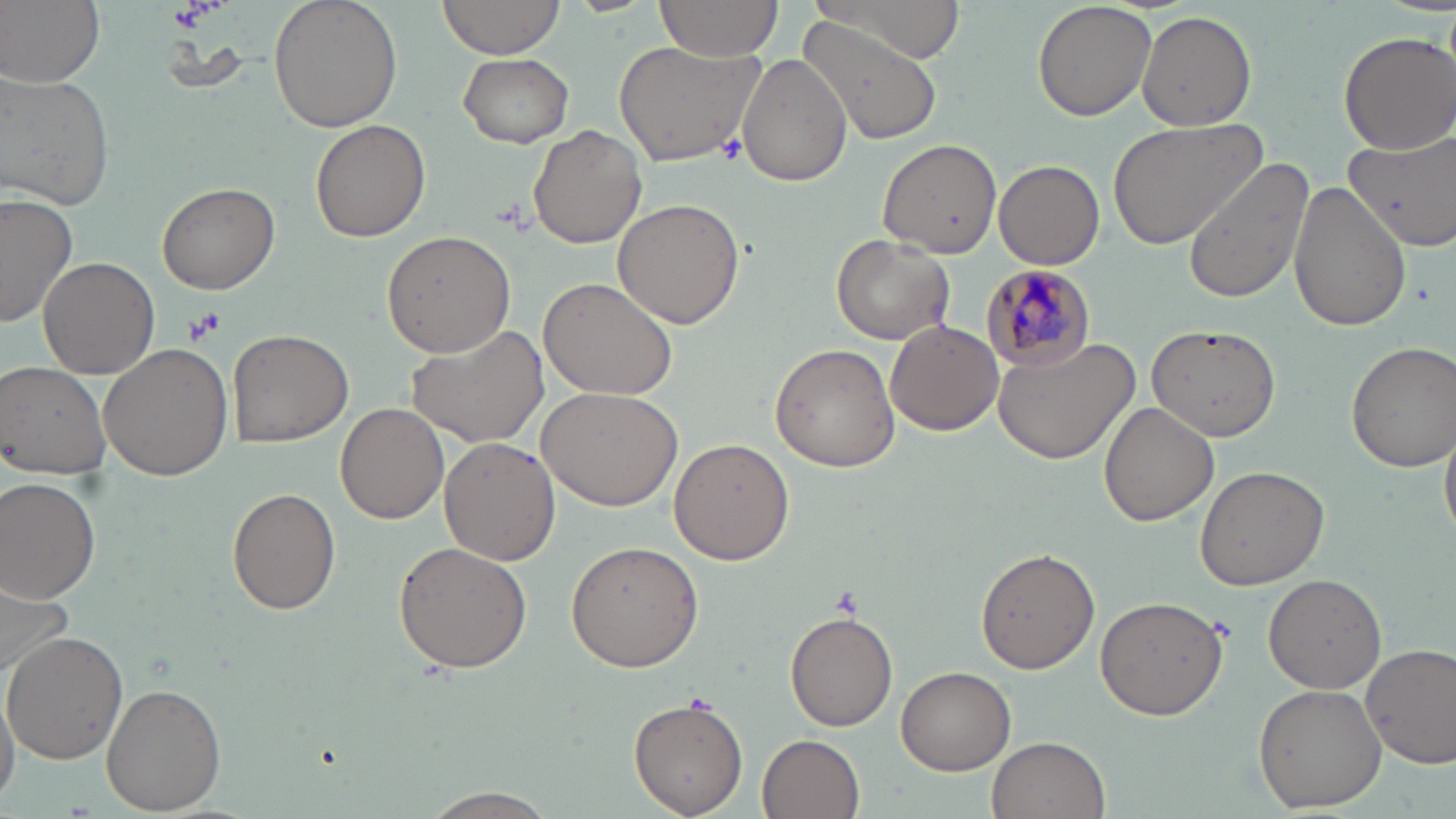
Approximate bounding boxes as (x1,y1)-(x2,y2) corner pairs in pixels. Plasmodium malariae-infected red blood cell locations: (978,261)-(1097,372). Uninfected red blood cell locations: (2,0)-(104,87), (267,0)-(403,134), (434,0)-(567,63), (652,0)-(786,67), (795,0)-(969,63), (1031,0)-(1157,121), (1136,10)-(1256,130), (796,13)-(944,147), (1336,31)-(1455,154), (612,38)-(768,169), (456,53)-(573,148), (737,54)-(851,185), (0,69)-(116,213), (1108,116)-(1263,250), (311,120)-(430,242), (528,124)-(648,249), (1342,126)-(1456,254), (877,138)-(1004,258), (1181,157)-(1316,304), (994,160)-(1104,269), (1288,178)-(1413,333), (157,182)-(279,294), (0,193)-(77,333), (614,198)-(745,328), (381,229)-(515,356), (830,234)-(956,345), (40,254)-(160,378), (539,275)-(677,400), (885,319)-(1004,435), (1142,322)-(1280,449), (404,325)-(549,450), (226,327)-(353,447), (993,334)-(1138,463), (1346,342)-(1456,470), (98,343)-(233,481), (769,343)-(900,472), (0,361)-(113,481), (537,385)-(683,511), (336,401)-(448,525), (1100,402)-(1218,526), (1440,422)-(1456,546), (440,438)-(559,567), (669,439)-(796,565), (1195,465)-(1329,590), (0,477)-(102,602), (227,487)-(341,614), (394,539)-(533,671), (566,540)-(703,673), (976,548)-(1099,674), (1262,575)-(1386,692), (0,578)-(76,686), (1094,596)-(1228,719), (784,609)-(898,732), (3,633)-(129,765), (1362,642)-(1456,766), (896,666)-(1016,775), (0,684)-(23,805), (1253,684)-(1385,809), (103,685)-(226,813), (629,694)-(748,817), (757,734)-(865,818), (987,735)-(1112,819), (418,787)-(560,818). Platelet locations: (716,136)-(747,165), (184,309)-(224,344). Slide-level diagnosis: Plasmodium malariae. 1000x magnification. Image is 1456×819 pixels. May-Grünwald-Giemsa stain. Single field of view. Optical microscopy. Thin blood film.